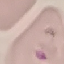
Summary:
  - Result: malaria parasites identified
  - Preparation: thin smear
  - Stain: Giemsa
  - Image type: automatically extracted cell patch, resized to 64 × 64 pixels
  - Capture: smartphone through the microscope eyepiece